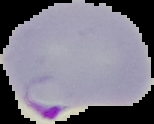

image size = 154×124 pixels
preparation = thin blood film
malaria status = parasitized
image type = cell region segmented out of the field of view; surrounding area masked to black